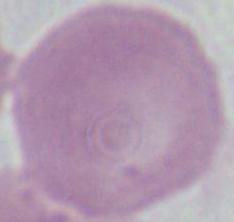
{
  "identification": "erythrocyte",
  "modality": "micrograph",
  "magnification": "1000x"
}